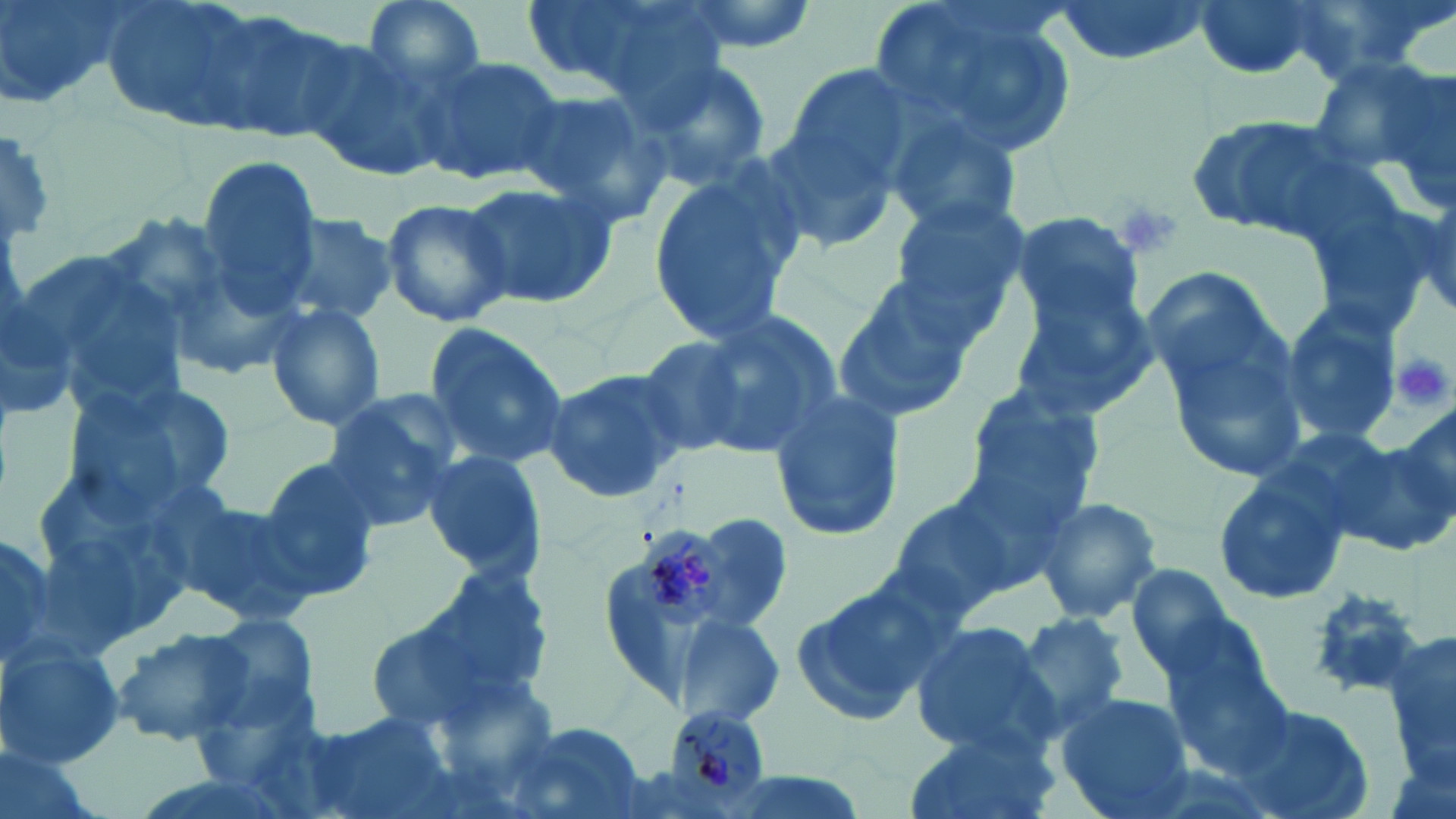

Approximate bounding boxes as (x1,y1)-(x2,y2) corner pairs in pixels. Uninfected red blood cell locations: (0,0)-(135,105), (97,0)-(288,138), (360,0)-(487,95), (525,0)-(726,107), (663,0)-(820,57), (864,0)-(1083,167), (1048,0)-(1213,64), (1191,0)-(1325,81), (1287,0)-(1446,82), (211,11)-(354,141), (295,38)-(449,184), (416,53)-(563,184), (1307,54)-(1451,186), (638,58)-(772,187), (785,64)-(915,184), (510,83)-(669,223), (885,108)-(1026,238), (1179,109)-(1358,240), (763,119)-(900,249), (194,155)-(324,310), (644,160)-(809,348), (459,178)-(618,313), (886,194)-(1030,334), (378,196)-(514,326), (1010,212)-(1146,325), (276,213)-(400,327), (11,238)-(190,424), (1136,264)-(1288,401), (829,277)-(979,425), (1009,285)-(1160,419), (1279,300)-(1403,445), (263,301)-(387,431), (1157,306)-(1310,480), (660,310)-(843,465), (423,324)-(570,470), (628,334)-(763,459), (540,368)-(690,504), (70,377)-(239,515), (961,384)-(1103,519), (767,387)-(908,544), (321,395)-(462,529), (1389,405)-(1456,530), (1325,437)-(1456,554), (417,450)-(546,579), (255,458)-(383,601), (1211,469)-(1352,607), (881,491)-(1030,622), (1033,494)-(1164,624), (176,497)-(322,625), (690,512)-(793,626), (0,523)-(62,673), (1125,568)-(1257,686), (787,576)-(955,729), (367,577)-(555,734), (1304,585)-(1434,701), (194,612)-(323,737), (675,613)-(786,728), (1014,613)-(1133,731), (1384,620)-(1456,791), (909,621)-(1058,758), (110,624)-(255,746), (0,640)-(125,769), (1162,646)-(1301,778), (1053,692)-(1195,819), (1230,703)-(1373,819), (299,712)-(450,819), (497,720)-(646,819), (897,728)-(1058,819). Platelet locations: (1118,203)-(1183,262), (1392,353)-(1451,412). Plasmodium malariae-infected red blood cell locations: (634,525)-(733,631), (652,707)-(776,808). Slide-level diagnosis: Plasmodium malariae. Thin blood film. 1000x magnification. One field of a larger specimen. May-Grünwald-Giemsa-stained preparation. Image is 1456×819 pixels. Optical microscopy.